Assess this cell for malaria.
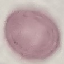

Uninfected.

Summary:
  - Stain: Giemsa
  - Preparation: thin blood smear
  - Image type: cell patch, automatically extracted from a larger field of view and resized to 64 × 64 pixels
  - Capture: smartphone through the microscope eyepiece